Assess this cell for malaria.
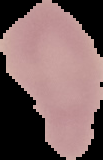
Uninfected.

{
  "preparation": "thin blood film",
  "image_size": "103×160 pixels",
  "image_type": "segmented cell region with the area outside set to black"
}